Assess the morphology of the erythrocytes.
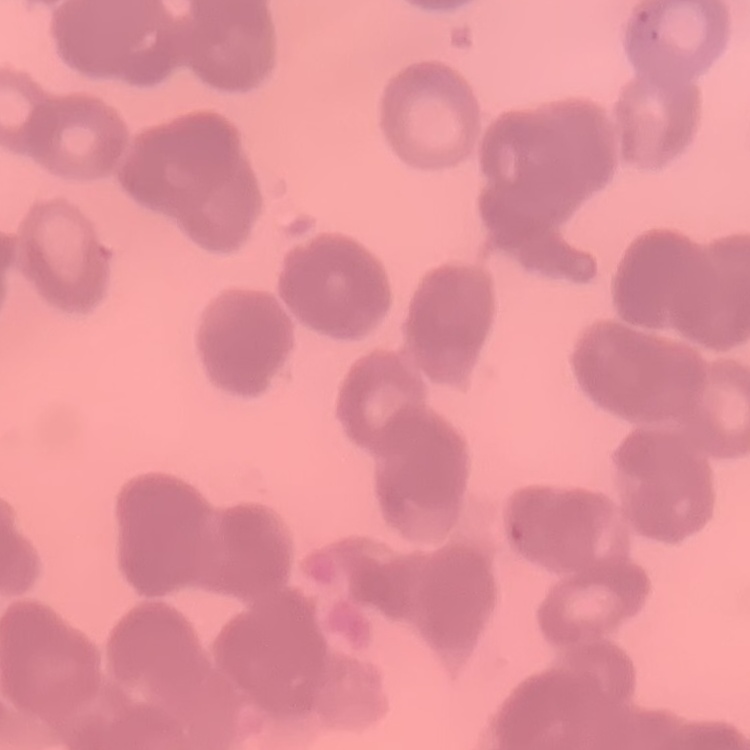
Rouleaux formation.

image type = one tile cut from a larger photomicrograph
stain = Field's or Giemsa
preparation = thin peripheral smear